Classify this cell by malaria status.
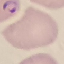
It is parasitized.

Thin blood film. Photographed with a smartphone camera at the microscope eyepiece. Cell patch, automatically extracted from a larger field of view and resized to 64 × 64 pixels. Giemsa stain.